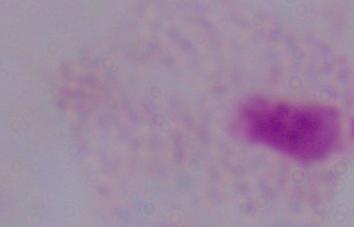
magnification: 1000x
modality: micrograph
identification: trichomonad